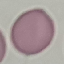
malaria status = uninfected
capture = smartphone through the microscope eyepiece
stain = Giemsa
preparation = thin blood smear
image type = automatically extracted cell patch, resized to 64 × 64 pixels